Identify the preparation type.
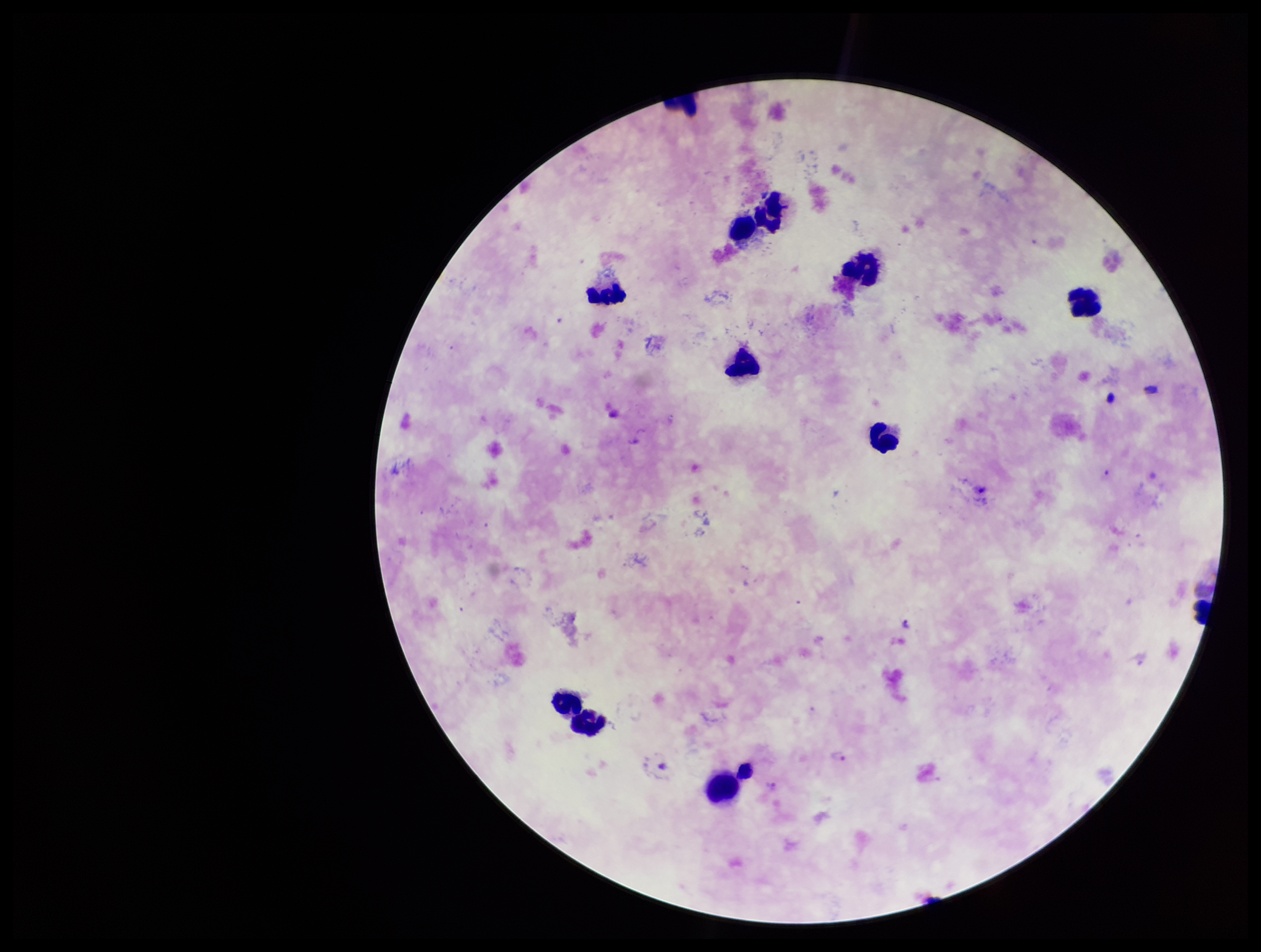
Thick.

capture = smartphone photograph through the microscope eyepiece
Plasmodium parasites = detected
species reported for this patient = Plasmodium vivax
leukocyte count = 11
patient malaria status = infected
parasite count = 2
stain = Giemsa
image size = 1261×952 pixels
field of view = one from this slide